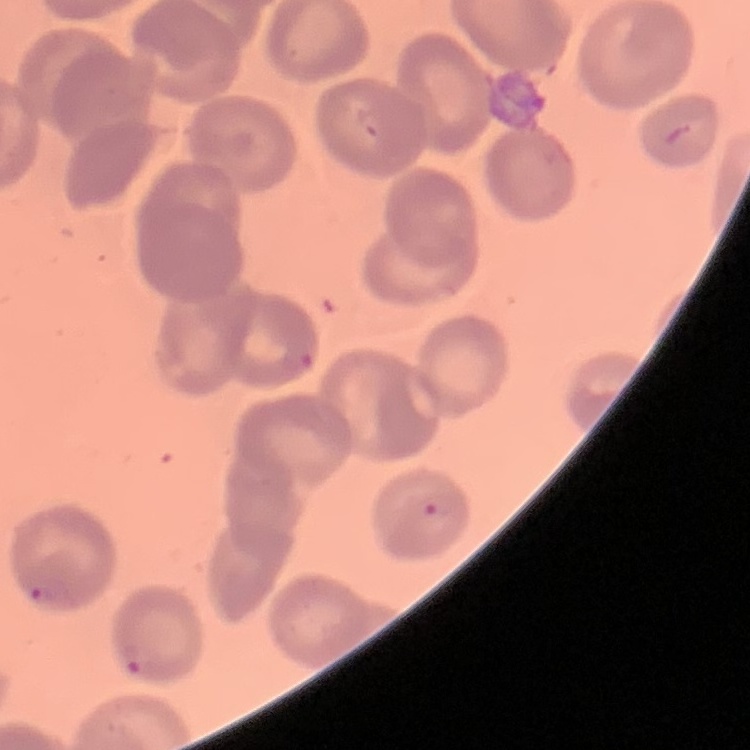

erythrocyte morphology = no rouleaux formation
stain = Field's or Giemsa
image type = one tile cut from a larger photomicrograph
preparation = thin blood smear